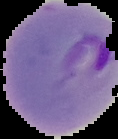

Summary:
  - Result: Plasmodium parasites identified
  - Preparation: thin blood smear
  - Image size: 118×139 pixels
  - Image type: segmented cell region with the area outside set to black